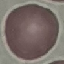
Malaria status: uninfected. Giemsa-stained preparation. Acquired by smartphone through the microscope eyepiece. Thin smear of blood. Cell patch, automatically extracted from a larger field of view and resized to 64 × 64 pixels.